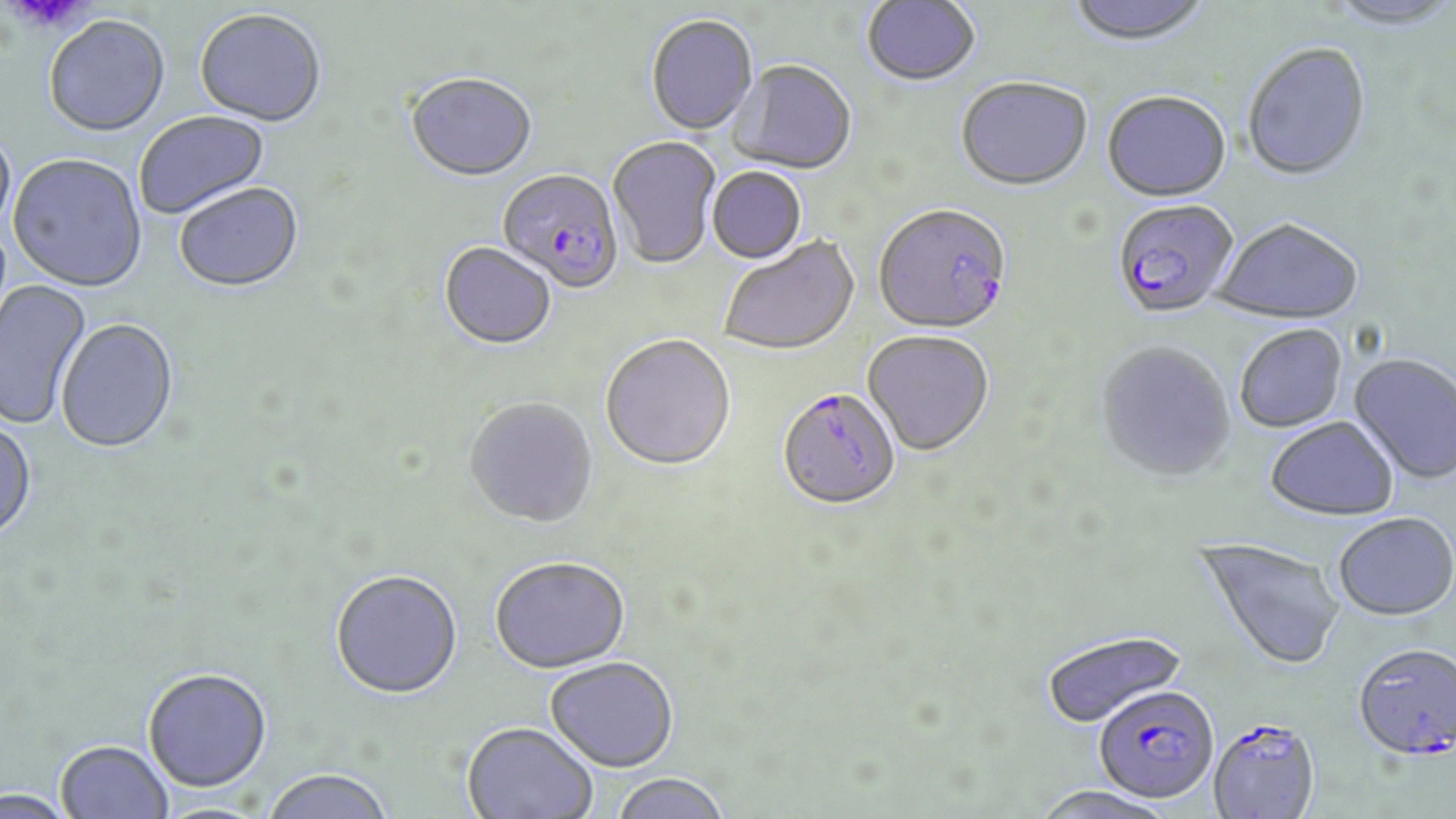
Approximate bounding boxes as (x1, y1, x2, y2) in pixels. Uninfected red blood cell locations: (1065, 0, 1213, 49), (861, 1, 982, 89), (1329, 2, 1456, 30), (194, 10, 326, 128), (645, 16, 758, 137), (43, 18, 170, 139), (1242, 45, 1373, 183), (729, 62, 857, 177), (404, 75, 537, 184), (955, 80, 1093, 194), (1102, 94, 1231, 204), (134, 111, 272, 221), (0, 128, 16, 241), (607, 136, 721, 271), (7, 155, 148, 295), (707, 168, 808, 266), (174, 185, 305, 295), (1213, 221, 1363, 328), (718, 236, 860, 358), (439, 244, 556, 351), (0, 278, 93, 430), (56, 320, 179, 455), (1235, 326, 1347, 434), (862, 333, 994, 458), (599, 336, 736, 474), (1096, 343, 1237, 486), (1348, 354, 1456, 486), (464, 398, 598, 530), (1265, 419, 1400, 523), (0, 420, 37, 543), (1333, 516, 1456, 624), (1194, 536, 1344, 673), (489, 559, 631, 676), (330, 571, 463, 702), (1040, 629, 1187, 729), (545, 658, 680, 773), (143, 670, 272, 796), (461, 723, 597, 819), (55, 742, 173, 819), (262, 770, 395, 819), (609, 774, 732, 819), (1028, 787, 1175, 819), (0, 791, 75, 819). Plasmodium falciparum-infected red blood cell locations: (497, 170, 624, 295), (1112, 201, 1239, 321), (873, 206, 1013, 338), (777, 390, 901, 513), (1354, 645, 1456, 765), (1093, 685, 1219, 805), (1207, 720, 1320, 818). Platelet locations: (12, 0, 92, 31). Slide-level diagnosis: Plasmodium falciparum. Thin blood smear. Captured at 1000x magnification. Image is 1456×819 pixels. Light microscopy. May-Grünwald-Giemsa-stained preparation. Single field of view.